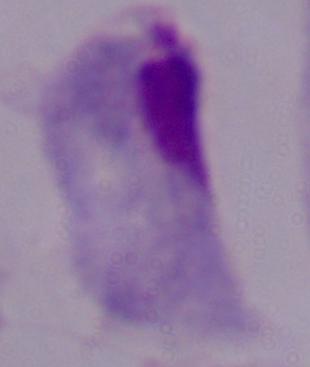
magnification = 1000x
identification = trichomonad
modality = micrograph